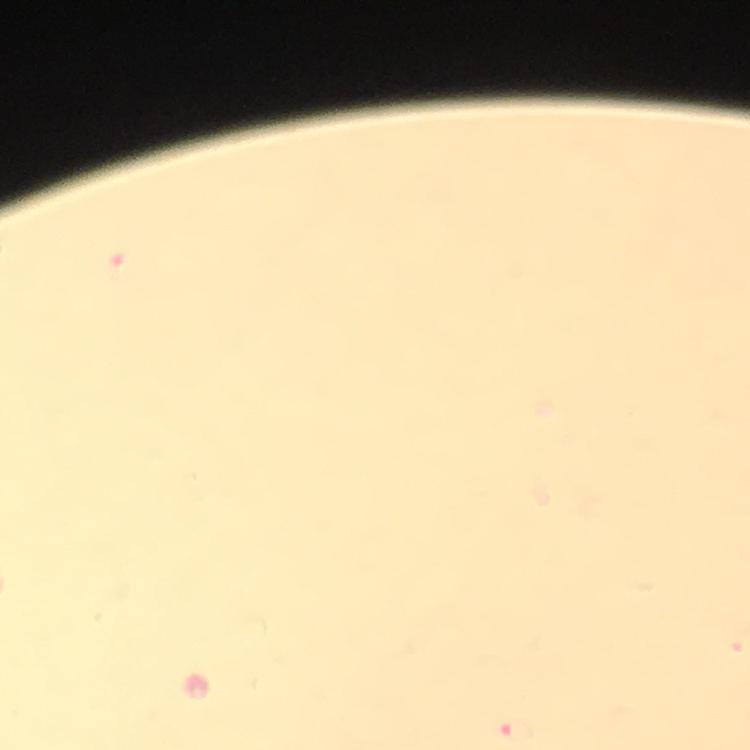

Approximate centers as (x, y) in pixels.
Summary:
  - Malaria parasite locations: (515, 730)
  - Context: from a malaria diagnostic workup
  - Image size: 750×750 pixels
  - Magnification: 100x
  - Capture: smartphone photograph through a microscope
  - Cropped from: a single field of view
  - Stain: Giemsa
  - Immersion oil: used
  - Preparation: thick blood smear